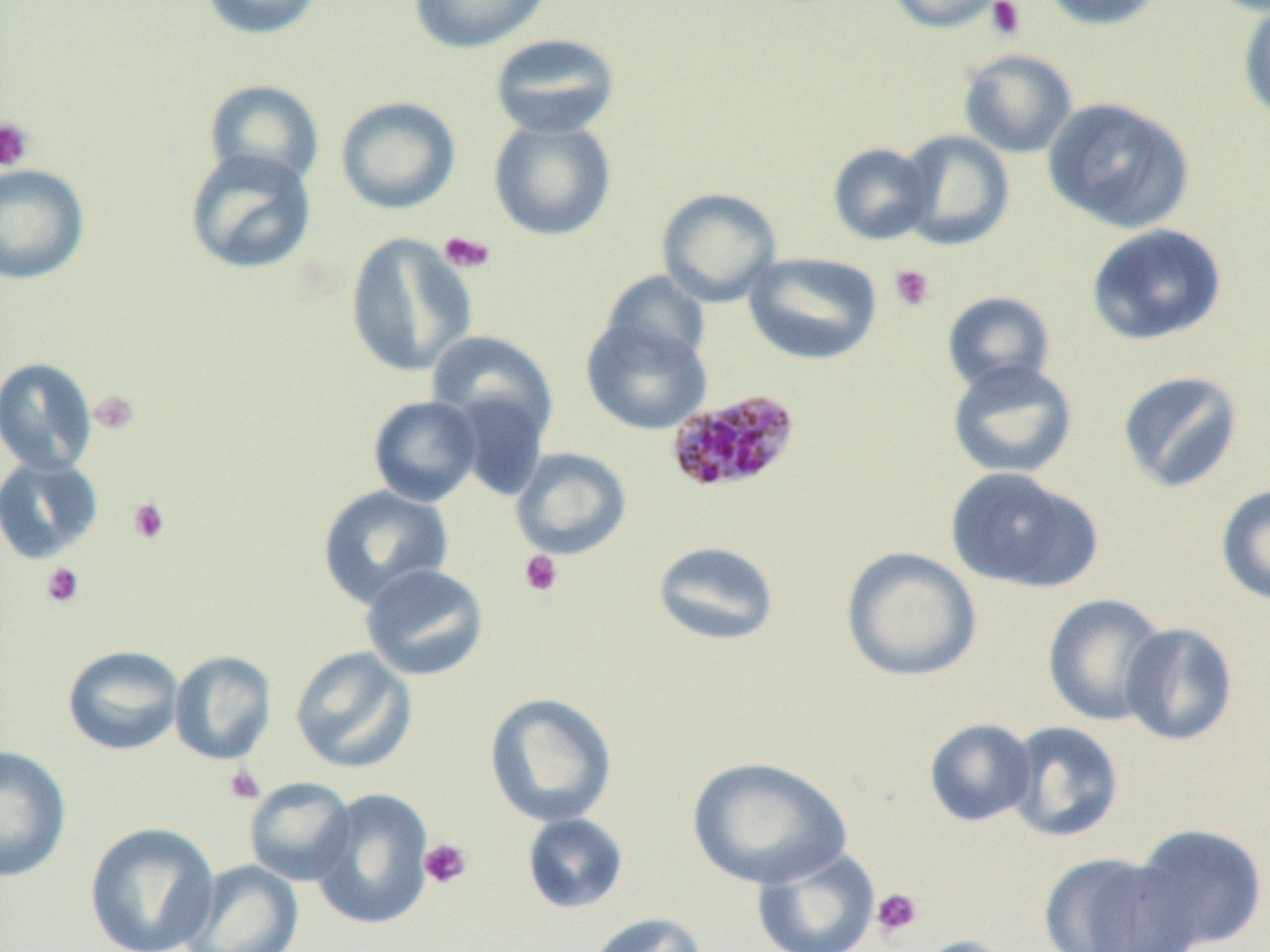 Approximate bounding boxes as [x1, y1, x2, y2] in pixels. Plasmodium malariae-infected red blood cell locations: [665, 388, 803, 495]. Uninfected red blood cell locations: [198, 0, 326, 41], [409, 0, 552, 54], [886, 0, 1008, 33], [1040, 0, 1166, 31], [1237, 2, 1270, 127], [489, 32, 621, 140], [958, 48, 1077, 159], [204, 79, 324, 188], [336, 96, 461, 215], [1042, 96, 1195, 234], [489, 118, 616, 241], [898, 130, 1015, 250], [827, 142, 934, 245], [184, 147, 318, 276], [0, 164, 90, 285], [656, 187, 782, 307], [1085, 224, 1228, 346], [345, 233, 477, 378], [744, 251, 883, 365], [599, 272, 712, 372], [942, 291, 1056, 394], [581, 315, 712, 435], [425, 329, 558, 443], [0, 356, 98, 475], [946, 359, 1078, 480], [1116, 370, 1244, 493], [446, 386, 552, 501], [367, 395, 483, 507], [510, 447, 632, 560], [0, 454, 104, 564], [944, 466, 1099, 593], [316, 484, 454, 609], [1216, 484, 1270, 605], [652, 540, 780, 647], [841, 547, 982, 681], [359, 563, 489, 682], [1042, 593, 1169, 726], [1120, 622, 1238, 746], [62, 644, 184, 756], [289, 646, 418, 774], [169, 650, 277, 766], [484, 692, 617, 827], [923, 718, 1038, 827], [1005, 721, 1125, 843], [0, 744, 72, 883], [686, 756, 852, 889], [244, 777, 357, 886], [309, 787, 435, 930], [521, 813, 629, 915], [84, 821, 220, 952], [1130, 822, 1269, 951], [751, 846, 881, 952], [1037, 851, 1199, 952], [181, 859, 305, 952], [585, 911, 708, 952], [906, 935, 1019, 952]. Platelet locations: [986, 0, 1026, 40], [0, 117, 34, 172], [438, 231, 495, 274], [889, 264, 935, 312], [88, 390, 140, 435], [127, 496, 170, 545], [518, 549, 564, 598], [40, 562, 86, 608], [222, 764, 265, 806], [419, 838, 472, 890], [871, 887, 924, 939]. Slide-level diagnosis: Plasmodium malariae. Image is 1270×952 pixels. Optical microscopy. Thin blood smear. Captured at 1000x magnification. One field of a larger specimen.